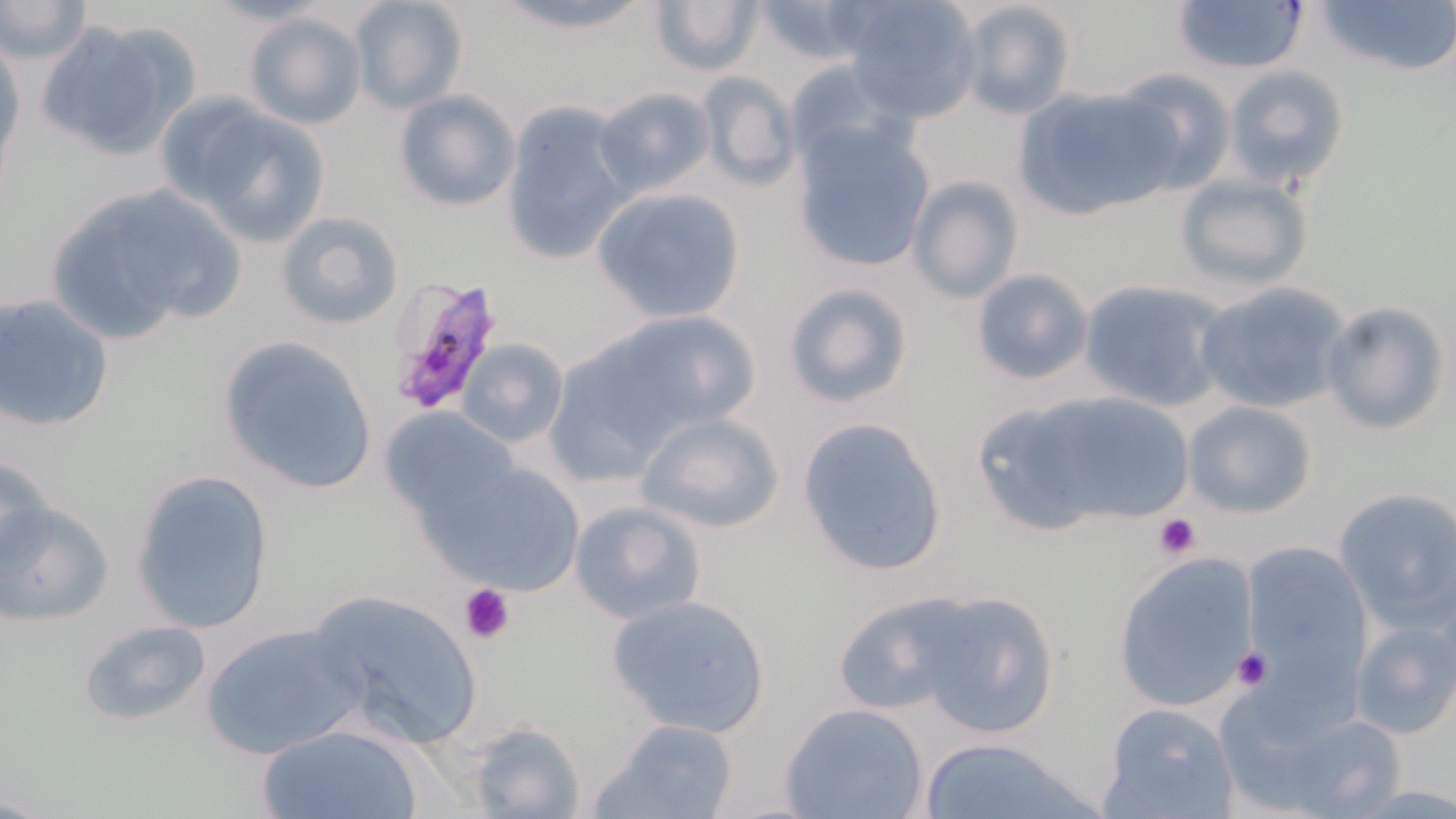
Approximate bounding boxes as [x1, y1, x2, y2] in pixels. Plasmodium falciparum-infected red blood cell locations: [384, 276, 507, 417]. Platelet locations: [1153, 512, 1201, 559], [458, 582, 514, 645], [1229, 645, 1274, 692]. Uninfected red blood cell locations: [347, 0, 468, 115], [485, 0, 666, 36], [742, 0, 880, 71], [839, 0, 981, 121], [1311, 0, 1456, 81], [1, 1, 93, 65], [650, 1, 762, 78], [1169, 1, 1311, 77], [952, 2, 1079, 121], [242, 10, 367, 130], [34, 16, 202, 164], [0, 32, 25, 187], [1224, 64, 1347, 188], [1108, 69, 1235, 199], [696, 72, 802, 192], [1014, 85, 1170, 219], [593, 86, 716, 201], [392, 90, 521, 212], [166, 98, 334, 245], [500, 103, 634, 267], [792, 123, 937, 273], [1172, 172, 1314, 293], [907, 175, 1023, 303], [42, 179, 244, 342], [589, 185, 747, 324], [276, 210, 405, 330], [970, 268, 1093, 386], [1077, 279, 1227, 413], [782, 281, 915, 411], [1193, 281, 1352, 415], [0, 295, 115, 433], [1321, 301, 1450, 435], [548, 314, 746, 475], [215, 334, 381, 498], [456, 340, 568, 447], [976, 386, 1193, 535], [1181, 400, 1318, 518], [377, 406, 519, 527], [635, 412, 783, 534], [796, 413, 949, 578], [417, 453, 588, 598], [134, 469, 274, 631], [1332, 486, 1456, 627], [1, 493, 113, 626], [569, 500, 705, 626], [1239, 541, 1373, 690], [1111, 550, 1263, 715], [304, 588, 484, 750], [866, 588, 1063, 736], [602, 593, 776, 738], [828, 596, 984, 716], [1347, 610, 1456, 742], [77, 617, 214, 725], [200, 622, 366, 759], [1220, 692, 1407, 819], [1100, 702, 1239, 819], [779, 703, 930, 819], [593, 718, 742, 819], [253, 722, 430, 819], [467, 724, 585, 819], [912, 737, 1107, 819]. Slide-level diagnosis: Plasmodium falciparum. Optical microscopy. 1000x magnification. Image is 1456×819 pixels. Thin blood film. Single field of view. May-Grünwald-Giemsa stain.